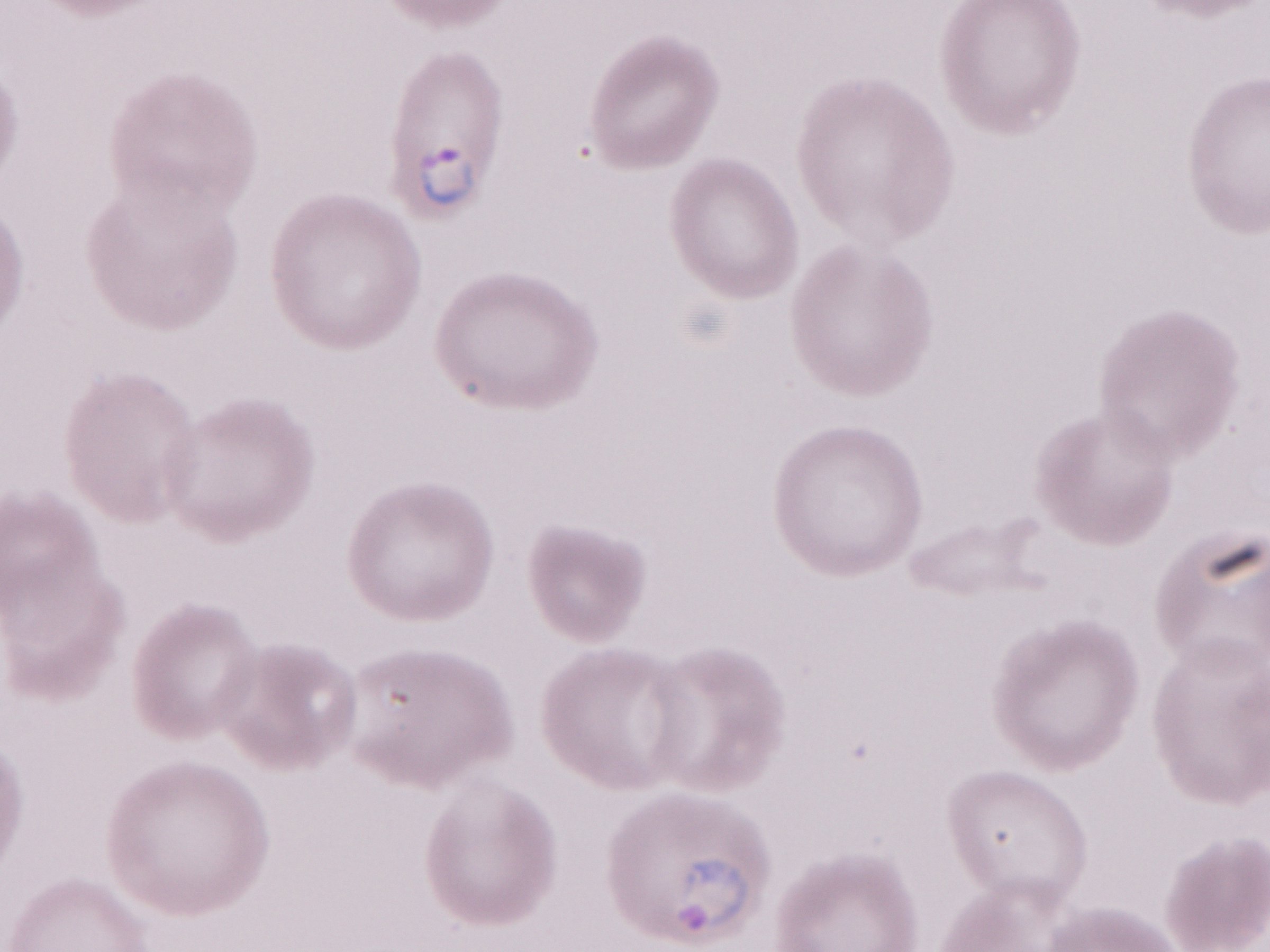
Thin blood film. May-Grünwald-Giemsa stain. Patient-level malaria diagnosis: positive. 1,000x magnification. Image is 1270×952 pixels. Olympus BX43 microscope and DP73 digital camera. Single field of view.